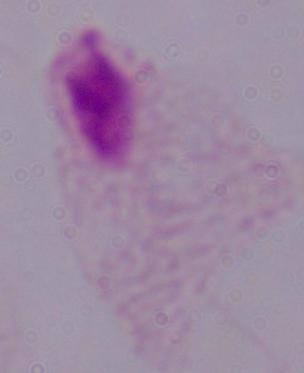
Micrograph. Captured at 1000x magnification. A trichomonad is shown.